Locate every Plasmodium ovale-infected red blood cell.
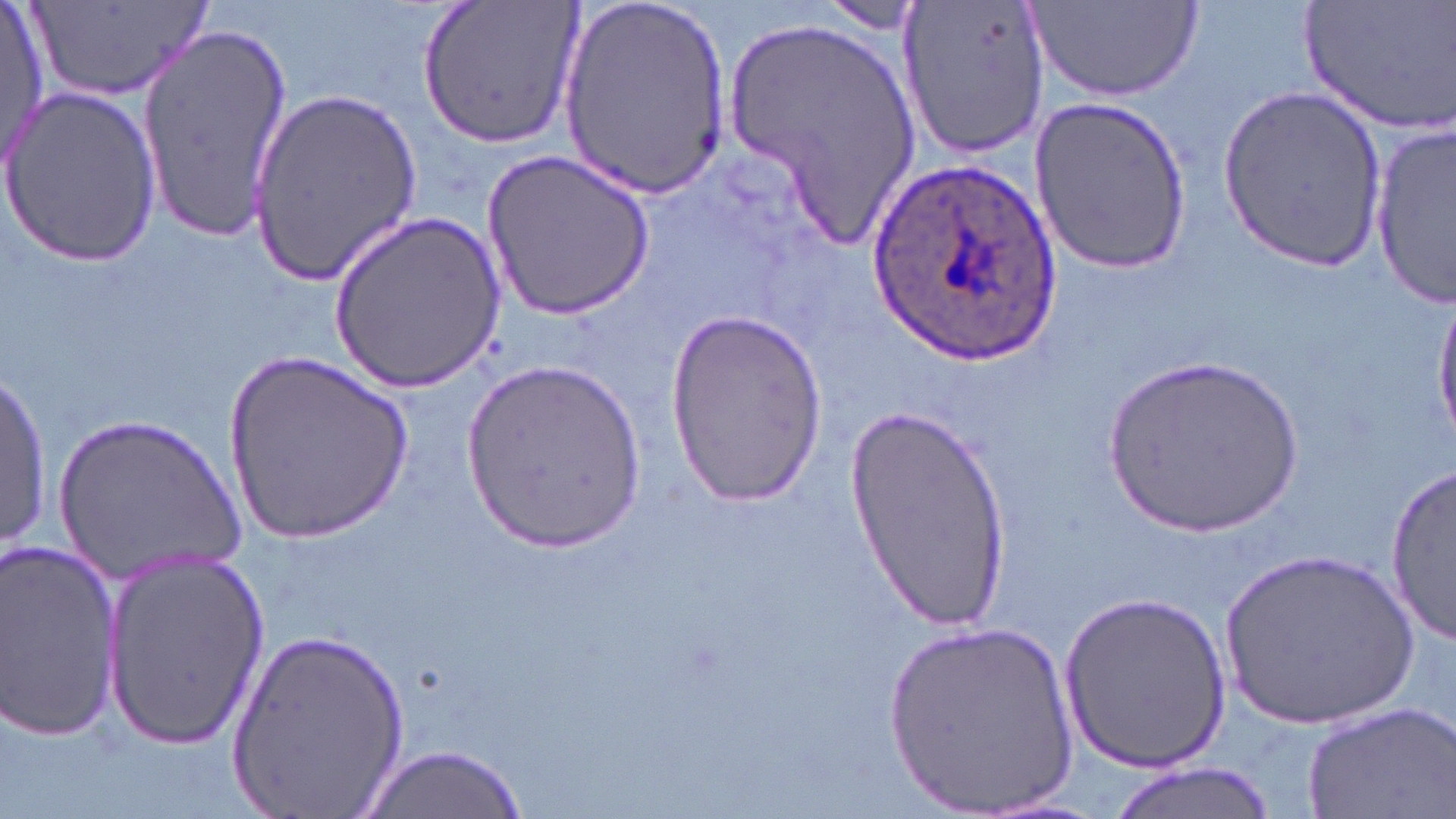

Approximate bounding boxes as (x1,y1)-(x2,y2) corner pairs in pixels.
Plasmodium ovale-infected red blood cells: (868,164)-(1063,366).

Summary:
  - Uninfected red blood cell locations: (0,0)-(49,175), (27,0)-(215,107), (415,0)-(584,152), (560,0)-(733,202), (897,0)-(1049,162), (1029,0)-(1204,102), (1302,0)-(1456,135), (815,3)-(926,35), (724,17)-(923,253), (137,23)-(295,240), (247,83)-(422,280), (1216,84)-(1387,270), (1,87)-(161,264), (1034,96)-(1193,275), (1369,124)-(1455,307), (482,149)-(659,319), (328,210)-(505,392), (1432,293)-(1456,444), (661,308)-(826,506), (226,353)-(413,545), (1104,353)-(1307,540), (463,358)-(643,554), (1,368)-(50,554), (844,402)-(1013,632), (50,412)-(243,580), (1381,464)-(1455,643), (0,537)-(124,741), (1221,546)-(1423,735), (100,550)-(269,750), (1059,591)-(1230,775), (880,616)-(1082,819), (229,625)-(411,818), (1297,701)-(1454,819), (353,743)-(527,819), (1108,763)-(1281,819)
  - Slide-level diagnosis: Plasmodium ovale
  - Modality: light microscopy
  - Preparation: thin blood film
  - Magnification: 1000x
  - Stain: May-Grünwald-Giemsa
  - Image size: 1456×819 pixels
  - Field of view: single